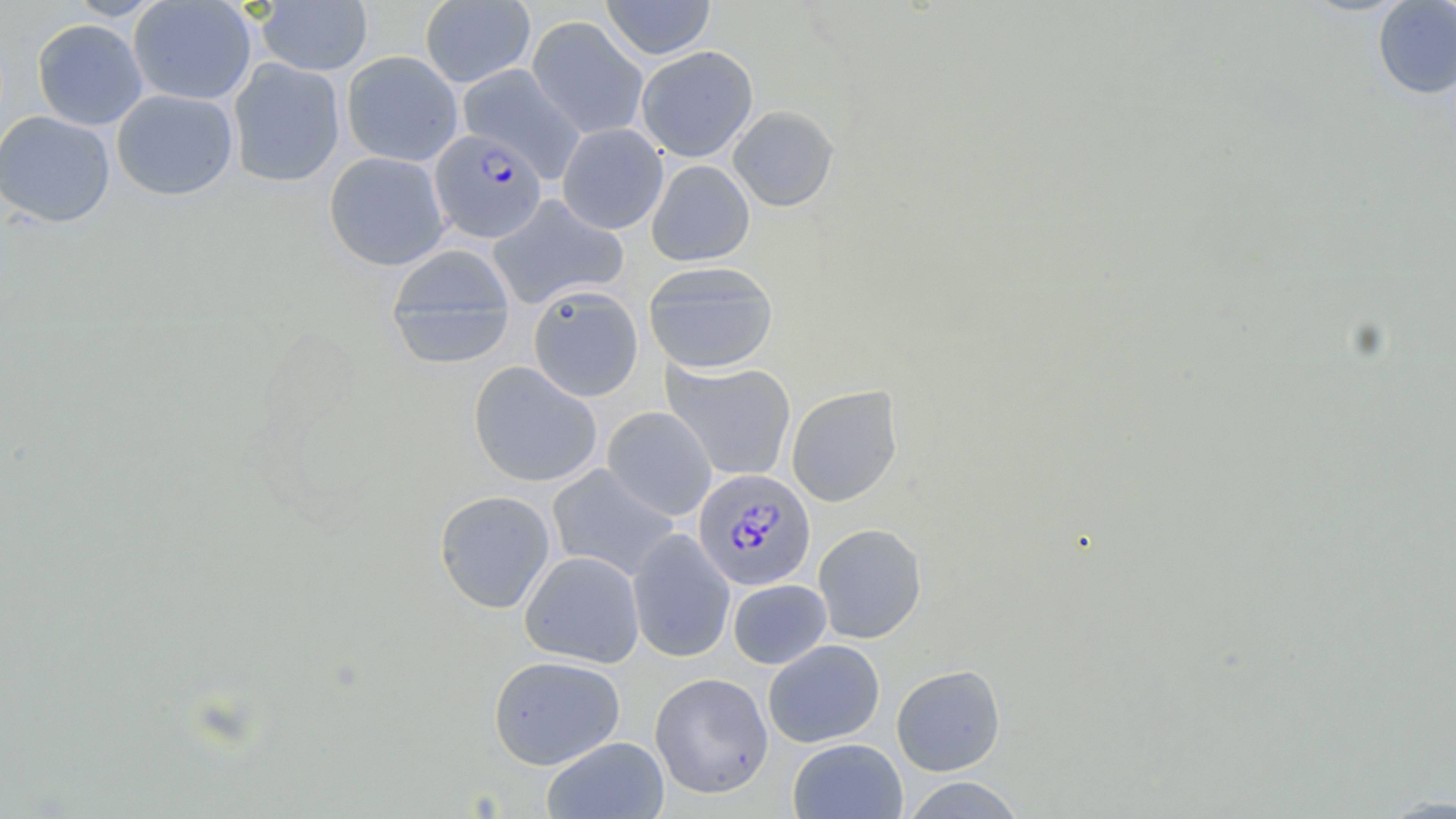
slide-level diagnosis = Plasmodium falciparum
stain = May-Grünwald-Giemsa
preparation = thin blood smear
uninfected red blood cell locations = approximate bounding boxes as [x1, y1, x2, y2] in pixels: [65, 0, 165, 20], [128, 0, 257, 105], [600, 0, 716, 60], [256, 1, 373, 76], [420, 1, 535, 88], [1372, 1, 1456, 99], [526, 15, 648, 140], [32, 19, 148, 131], [636, 46, 758, 162], [341, 50, 463, 167], [227, 58, 345, 187], [457, 64, 586, 181], [112, 89, 239, 200], [728, 104, 839, 212], [0, 110, 115, 227], [557, 123, 668, 234], [323, 151, 450, 270], [646, 160, 755, 266], [488, 194, 628, 310], [386, 244, 517, 368], [643, 261, 778, 374], [527, 285, 644, 401], [661, 358, 796, 481], [468, 361, 602, 488], [786, 385, 903, 507], [603, 406, 716, 520], [547, 464, 680, 582], [434, 484, 678, 600], [434, 489, 556, 614], [813, 523, 927, 644], [627, 529, 736, 663], [519, 550, 645, 668], [728, 579, 831, 669], [763, 639, 885, 748], [488, 655, 625, 769], [891, 664, 1006, 776], [650, 672, 774, 799], [541, 736, 669, 819], [788, 738, 907, 819], [900, 776, 1027, 818]
modality = optical microscopy
field of view = one of a larger specimen
image size = 1456×819 pixels
magnification = 1000x
Plasmodium falciparum-infected red blood cell locations = approximate bounding boxes as [x1, y1, x2, y2] in pixels: [429, 129, 547, 244], [693, 469, 816, 591]